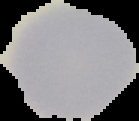

preparation = thin blood film
image type = segmented cell region on a black background
image size = 139×121 pixels
result = no Plasmodium parasites seen